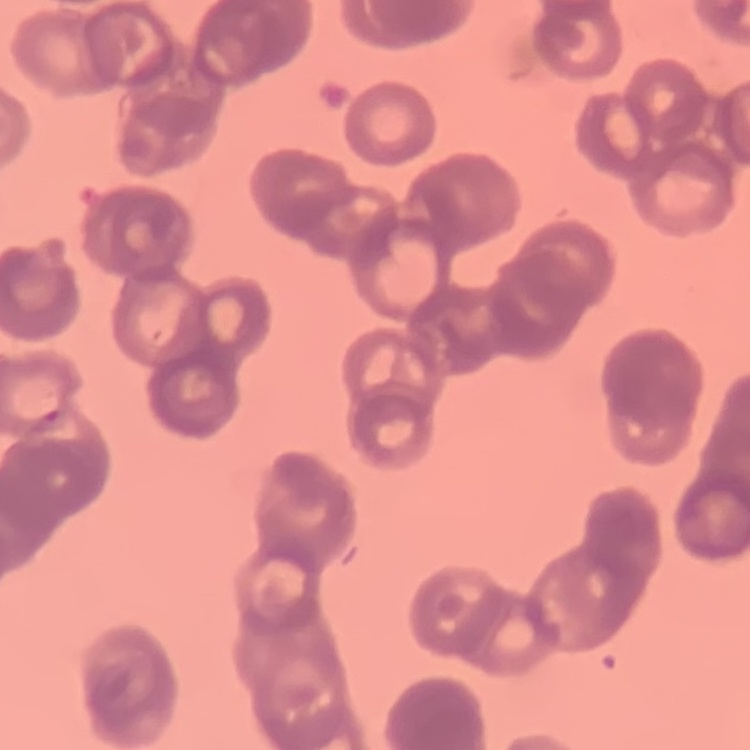
Summary:
  - Red blood cell morphology: rouleaux formation
  - Stain: Field's or Giemsa
  - Image type: square crop of a larger photomicrograph
  - Preparation: thin peripheral smear